Assess this cell for malaria.
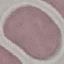
Uninfected.

Summary:
  - Image type: automatically extracted cell patch, resized to 64 × 64 pixels
  - Stain: Giemsa
  - Capture: smartphone through the microscope eyepiece
  - Preparation: thin smear